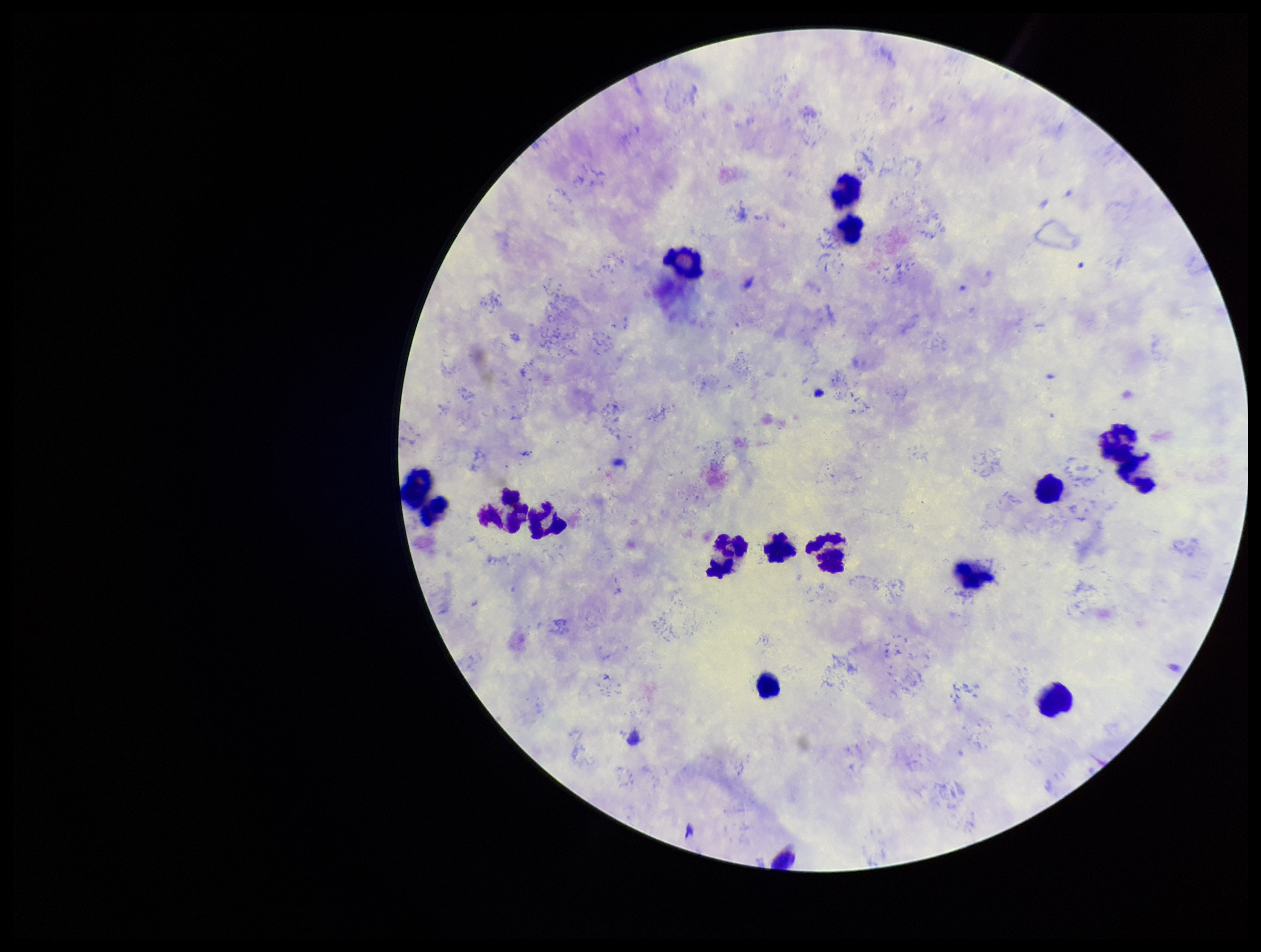

{
  "stain": "Giemsa",
  "preparation": "thick smear",
  "leukocyte_count": 13,
  "patient_malaria_status": "infected",
  "plasmodium_parasites": "none detected",
  "image_size": "1261×952 pixels",
  "field_of_view": "one from this slide",
  "species_reported_for_this_patient": "Plasmodium vivax",
  "parasite_count": 0,
  "capture": "smartphone photograph through the microscope eyepiece"
}